Assess this cell for malaria.
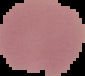

It is uninfected.

Summary:
  - Image size: 85×76 pixels
  - Preparation: thin blood film
  - Image type: cell region segmented out of the field of view; surrounding area masked to black